State which parasite is depicted.
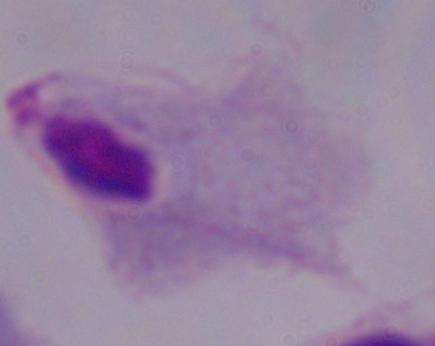

This is a trichomonad.

Summary:
  - Magnification: 1000x
  - Modality: micrograph